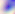

modality: photomicrograph
identification: Toxoplasma gondii
magnification: 400x